Assess the morphology of the erythrocytes.
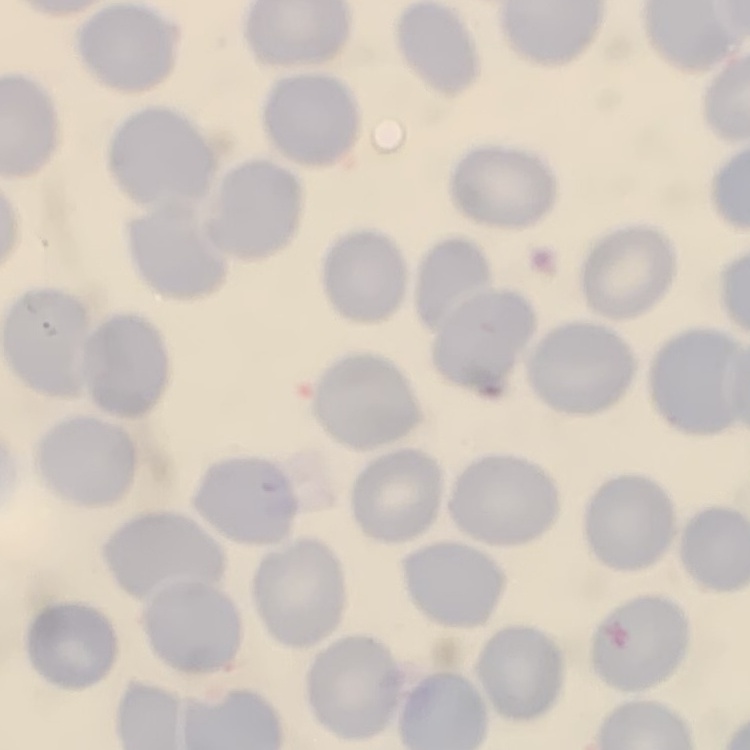

They show no rouleaux formation.

stain = Field's or Giemsa
preparation = thin blood smear
image type = square crop of a larger photomicrograph